Give the extent of all Plasmodium vivax-infected red blood cells.
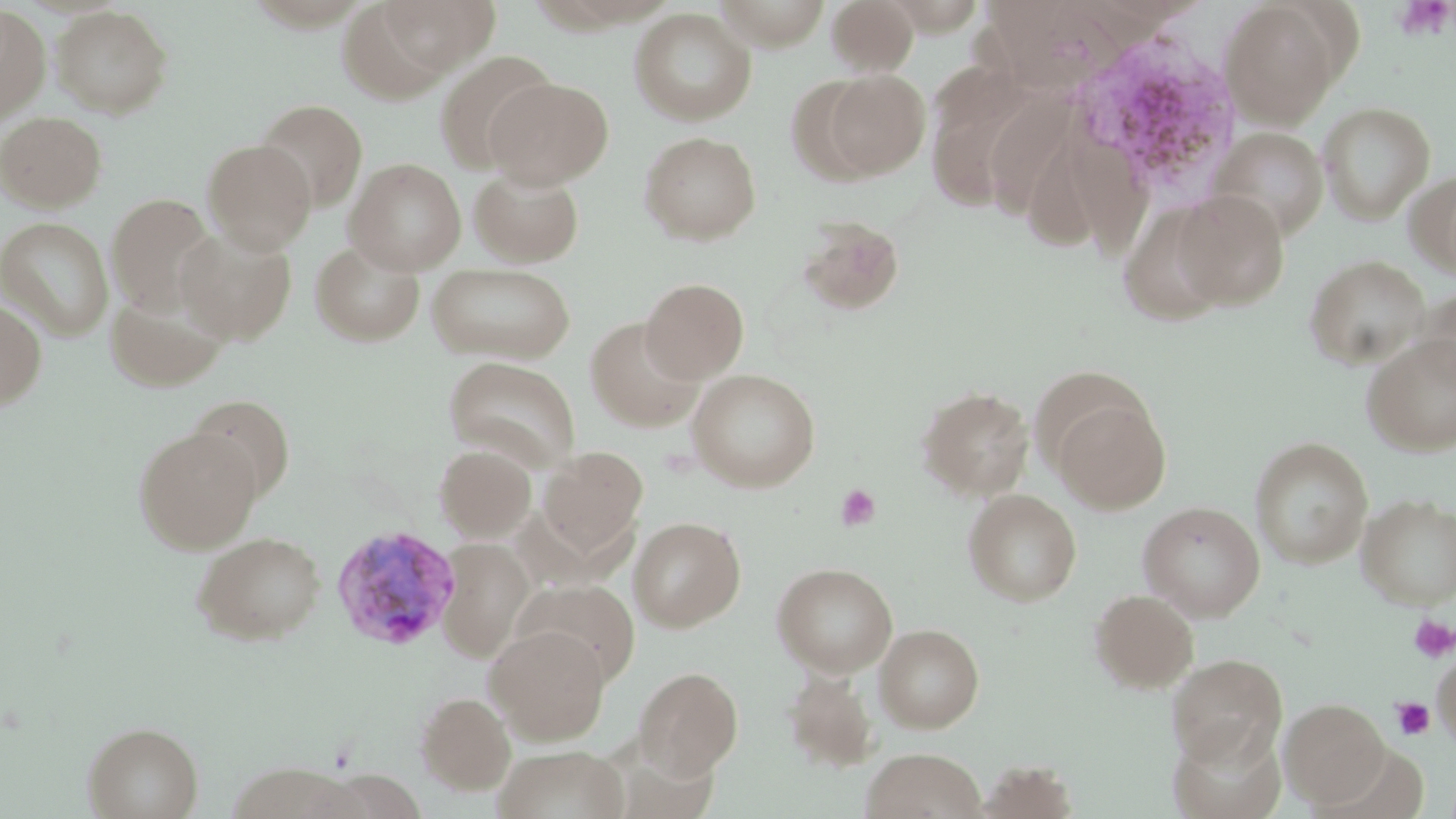

Approximate bounding boxes as (x1, y1, x2, y2) in pixels.
Plasmodium vivax-infected red blood cells: (330, 523, 460, 651).

Platelet locations: (1392, 0, 1454, 41), (835, 484, 881, 532), (1408, 615, 1455, 663), (1390, 696, 1436, 740). Uninfected red blood cell locations: (370, 0, 501, 78), (825, 0, 920, 76), (1219, 1, 1344, 127), (335, 2, 463, 104), (0, 4, 51, 123), (51, 5, 173, 117), (629, 7, 757, 125), (435, 50, 556, 174), (819, 69, 930, 179), (485, 76, 612, 189), (992, 92, 1083, 222), (937, 95, 1037, 217), (254, 99, 368, 211), (1317, 101, 1436, 224), (1067, 109, 1153, 262), (0, 111, 107, 212), (1208, 127, 1329, 240), (638, 130, 762, 245), (202, 139, 316, 254), (1024, 147, 1103, 252), (345, 158, 467, 274), (468, 165, 585, 268), (1409, 168, 1456, 282), (1170, 190, 1291, 311), (106, 193, 220, 316), (1122, 206, 1221, 332), (1, 215, 114, 340), (796, 217, 906, 317), (176, 226, 297, 344), (310, 238, 426, 347), (1303, 254, 1430, 371), (427, 262, 576, 364), (640, 277, 749, 382), (1414, 285, 1456, 393), (104, 290, 230, 391), (0, 299, 47, 412), (585, 316, 706, 433), (1360, 333, 1456, 455), (442, 355, 582, 471), (687, 368, 822, 491), (915, 384, 1034, 500), (1049, 393, 1171, 513), (186, 395, 295, 500), (133, 426, 263, 553), (1249, 436, 1373, 569), (434, 443, 537, 542), (536, 445, 648, 559), (963, 489, 1082, 606), (1356, 492, 1456, 609), (1137, 500, 1266, 621), (629, 516, 747, 632), (191, 530, 327, 645), (436, 538, 535, 661), (772, 562, 898, 677), (514, 580, 638, 686), (1089, 588, 1199, 693), (875, 623, 985, 732), (485, 625, 610, 745), (1431, 651, 1456, 747), (1166, 654, 1287, 767), (634, 666, 743, 778), (782, 667, 879, 773), (415, 690, 517, 795), (1280, 698, 1390, 808), (81, 721, 203, 819), (1169, 722, 1287, 819), (493, 746, 630, 819), (861, 747, 987, 819), (977, 760, 1078, 817). Slide-level diagnosis: Plasmodium vivax. Optical microscopy. Image is 1456×819 pixels. Single field of view. Thin blood film. Captured at 1000x magnification. May-Grünwald-Giemsa stain.